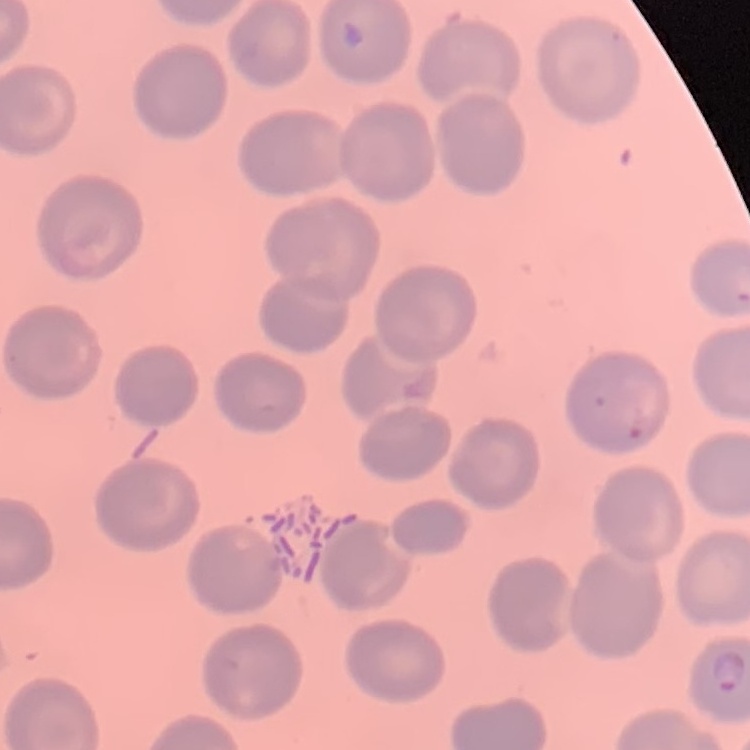

Summary:
  - Red blood cell morphology: no rouleaux formation
  - Preparation: thin blood smear
  - Image type: square crop of a larger photomicrograph
  - Stain: Field's or Giemsa